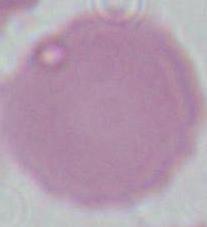

Summary:
  - Magnification: 1000x
  - Modality: micrograph
  - Identification: red blood cell